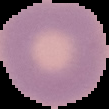

result = no Plasmodium parasites seen
image size = 109×109 pixels
preparation = thin blood film
image type = segmented cell region with the area outside set to black